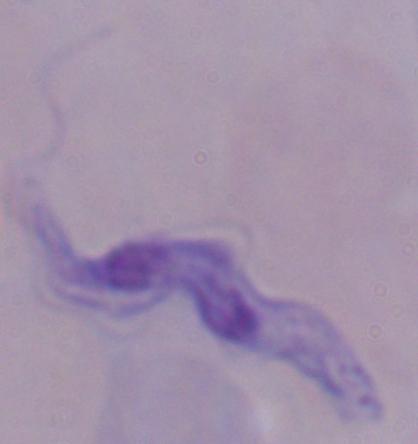
Summary:
  - Modality: micrograph
  - Identification: trypanosome
  - Magnification: 1000x